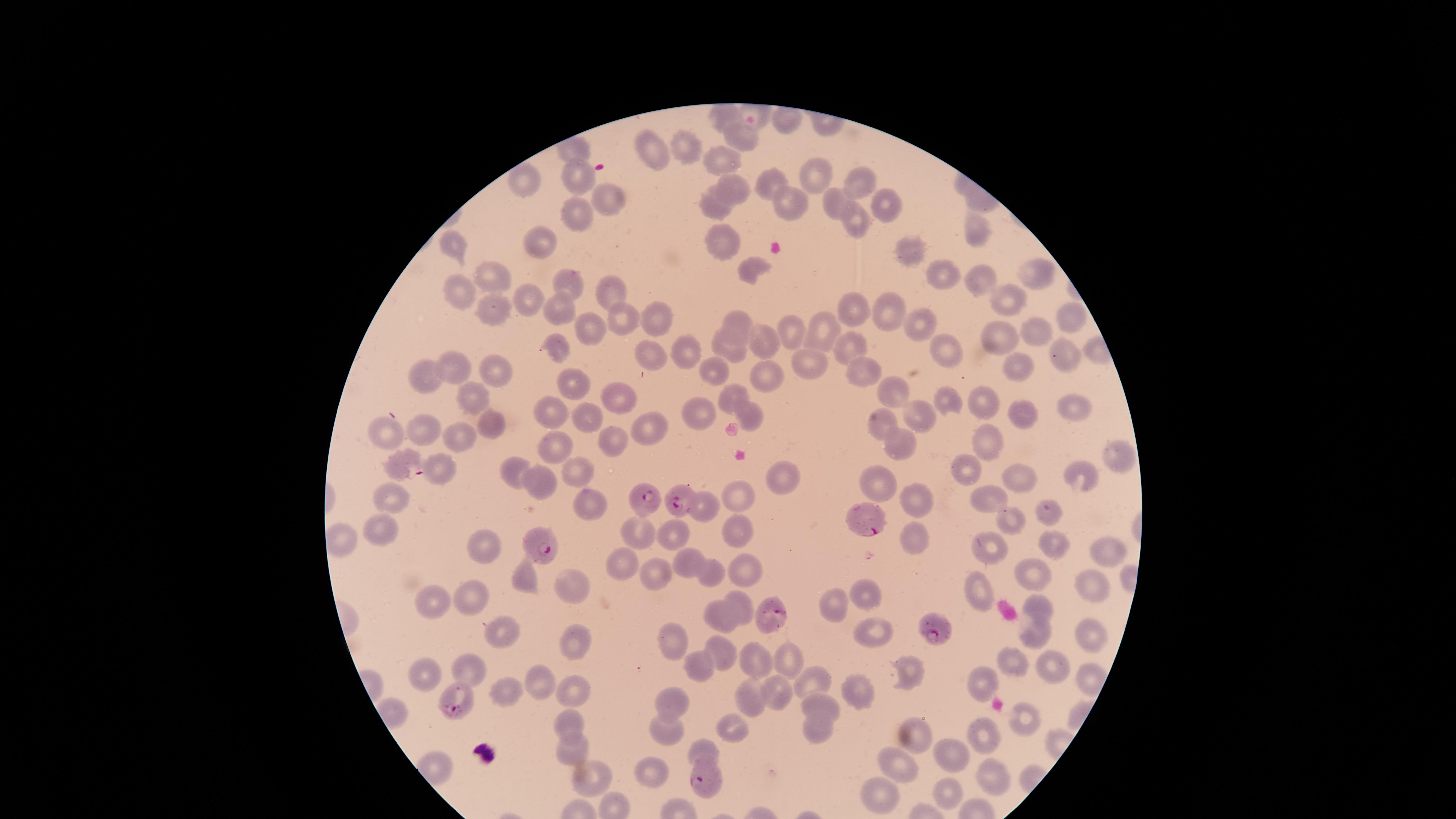

Approximate marker points as [x, y] in pixels.
Summary:
  - Uninfected RBCs: [740, 135], [687, 146], [652, 147], [719, 159], [574, 172], [820, 174], [521, 177], [852, 181], [728, 183], [610, 200], [832, 203], [882, 204], [715, 207], [573, 213], [855, 218], [977, 228], [724, 238], [542, 244], [450, 246], [915, 252], [1034, 270], [748, 272], [946, 274], [497, 275], [566, 278], [975, 281], [610, 290], [459, 293], [527, 297], [1006, 299], [856, 306], [489, 307], [558, 308], [891, 313], [1069, 314], [617, 315], [655, 316], [737, 322], [917, 323], [788, 328], [824, 330], [1043, 330], [586, 331], [1003, 336], [731, 341], [762, 342], [557, 343], [845, 344], [680, 348], [946, 354], [1065, 356], [649, 357], [806, 360], [1020, 365], [489, 368], [714, 368], [855, 369], [459, 370], [763, 372], [431, 375], [574, 381], [897, 390], [729, 392], [476, 395], [616, 397], [946, 401], [985, 401], [1070, 402], [691, 407], [549, 410], [589, 413], [747, 413], [1026, 413], [925, 415], [879, 422], [494, 424], [646, 425], [423, 427], [382, 432], [460, 439], [986, 439], [897, 440], [618, 443], [556, 448], [1110, 459], [966, 463], [439, 468], [513, 468], [573, 473], [1020, 473], [1075, 475], [777, 477], [877, 479], [548, 488], [915, 493], [737, 494], [391, 495], [988, 496], [586, 507], [702, 508], [1051, 511], [1014, 521], [734, 529], [380, 530], [631, 532], [676, 533], [340, 539], [917, 539], [483, 542], [1052, 544], [993, 550], [1103, 551], [687, 558], [616, 563], [747, 570], [711, 572], [1031, 572], [652, 575], [527, 576], [573, 581], [1086, 585], [977, 590], [469, 593], [867, 595], [744, 600], [434, 602], [835, 605], [1038, 606], [723, 611], [507, 632], [874, 632], [1090, 635], [1033, 636], [677, 637], [574, 640], [718, 647], [747, 657], [785, 660], [1009, 660], [701, 666], [1051, 666], [468, 668], [424, 670], [907, 670], [1090, 677], [539, 679], [985, 679], [811, 680], [781, 690], [856, 690], [576, 691], [752, 692], [509, 693], [673, 697], [818, 704], [568, 719], [1023, 719], [733, 726], [668, 728], [816, 729], [983, 734], [917, 740], [706, 748], [952, 750], [569, 752], [900, 765], [987, 769], [652, 771], [590, 777], [946, 791], [878, 797]
  - Parasitized RBCs: [405, 463], [683, 499], [645, 502], [865, 519], [542, 543], [766, 613], [936, 626], [458, 697], [706, 781]
  - Stain: Giemsa
  - Species: Plasmodium falciparum
  - Field of view: single
  - Visible region: circular
  - Image size: 1456×819 pixels
  - Preparation: thin blood smear
  - Capture: smartphone photograph through the microscope eyepiece
  - Presence: malaria parasites detected